Point out each Plasmodium parasite.
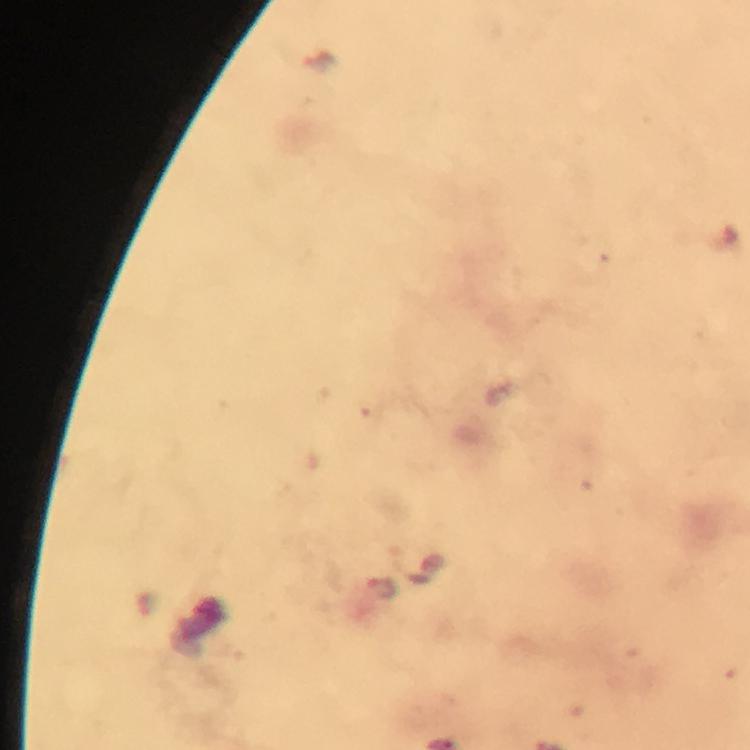

Approximate object centers, in pixels from the top-left corner.
Plasmodium parasites: (x=381, y=586).

Summary:
  - Stain: Giemsa
  - Context: from a malaria diagnostic workup
  - Magnification: 100x
  - Cropped from: a single field of view
  - Capture: smartphone mounted on the microscope
  - Image size: 750×750 pixels
  - Preparation: thick blood smear
  - Immersion oil: used